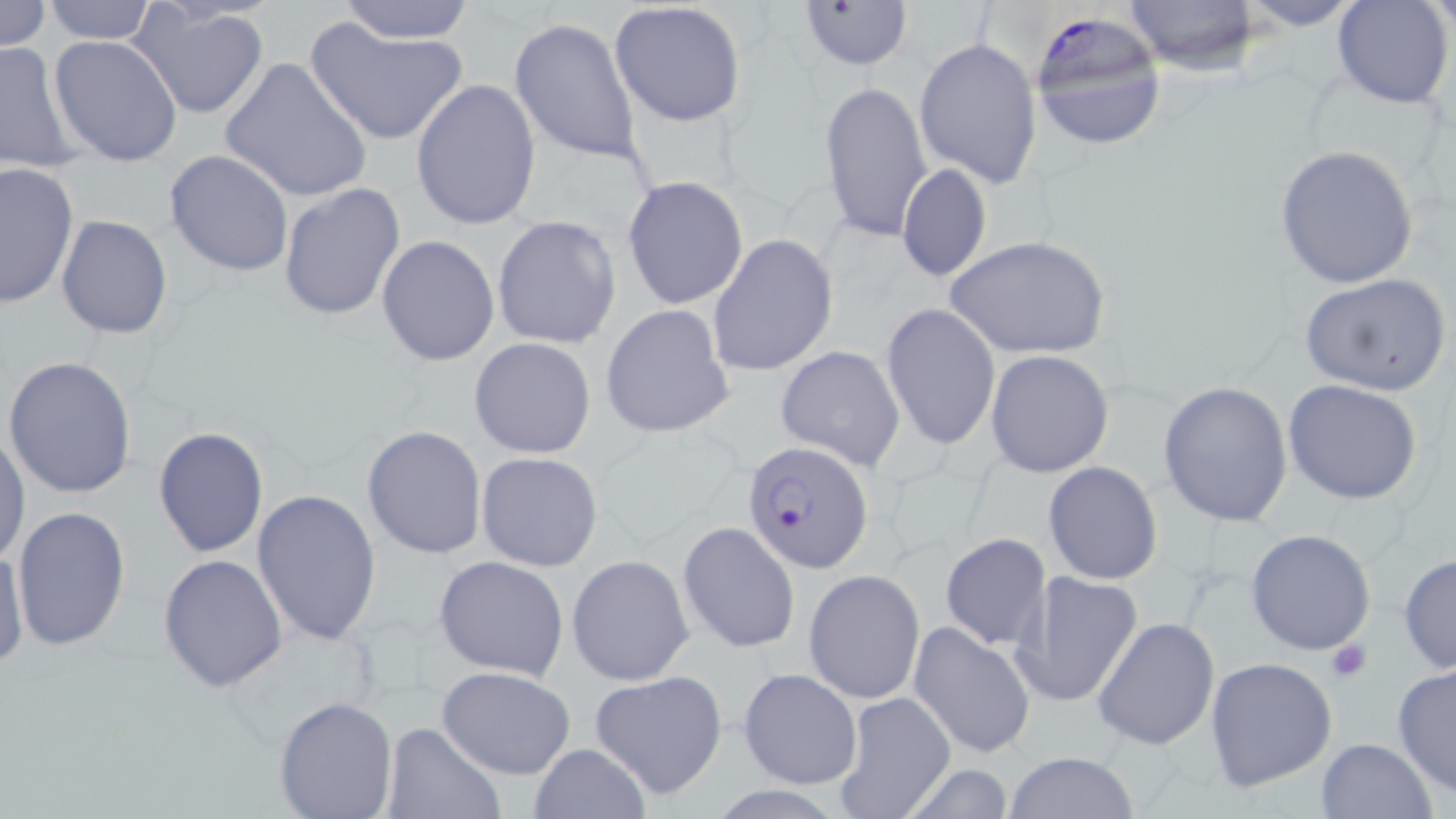

Approximate bounding boxes as (x1, y1, x2, y2) in pixels. Plasmodium falciparum-infected red blood cell locations: (1029, 11, 1168, 151), (742, 439, 875, 574). Uninfected red blood cell locations: (0, 0, 51, 55), (39, 0, 163, 44), (1121, 0, 1262, 76), (1229, 0, 1370, 31), (1333, 0, 1453, 109), (796, 1, 912, 70), (332, 2, 479, 43), (608, 2, 747, 129), (127, 3, 270, 119), (305, 16, 472, 146), (509, 18, 643, 164), (49, 35, 182, 166), (914, 37, 1041, 189), (0, 38, 86, 178), (220, 57, 372, 203), (411, 78, 541, 231), (820, 80, 932, 246), (1276, 145, 1421, 290), (165, 150, 293, 278), (0, 161, 78, 308), (895, 163, 993, 284), (622, 176, 749, 309), (278, 183, 405, 323), (56, 214, 173, 340), (491, 216, 621, 348), (708, 235, 838, 377), (376, 236, 499, 365), (949, 236, 1108, 360), (1299, 272, 1452, 398), (599, 304, 734, 438), (882, 304, 999, 451), (469, 336, 597, 459), (776, 342, 905, 471), (985, 349, 1115, 478), (3, 355, 138, 500), (1283, 379, 1424, 505), (1158, 381, 1293, 528), (362, 426, 486, 560), (153, 427, 269, 559), (1, 429, 29, 568), (476, 452, 604, 573), (1043, 460, 1162, 585), (251, 488, 381, 646), (11, 505, 131, 655), (677, 522, 799, 652), (1245, 528, 1375, 655), (940, 532, 1052, 650), (568, 540, 798, 668), (1, 543, 28, 671), (1397, 553, 1456, 675), (157, 554, 288, 693), (433, 554, 571, 679), (566, 554, 694, 687), (803, 569, 924, 704), (1013, 569, 1144, 708), (1094, 617, 1220, 752), (910, 621, 1037, 759), (1204, 656, 1337, 793), (1391, 662, 1456, 799), (436, 666, 576, 780), (738, 667, 863, 789), (589, 670, 728, 798), (833, 692, 956, 818), (274, 695, 398, 818), (379, 723, 507, 818), (1313, 737, 1437, 819), (527, 742, 653, 819), (1005, 751, 1140, 818), (895, 761, 1019, 818). Platelet locations: (1326, 638, 1373, 684). Slide-level diagnosis: Plasmodium falciparum. One field of a larger specimen. May-Grünwald-Giemsa stain. Image is 1456×819 pixels. Thin blood film. 1000x magnification. Light microscopy.